Report the malaria status of this cell.
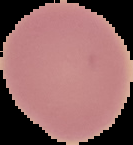
Uninfected.

preparation = thin blood smear
image size = 133×145 pixels
image type = cell region segmented out of the field of view; surrounding area masked to black